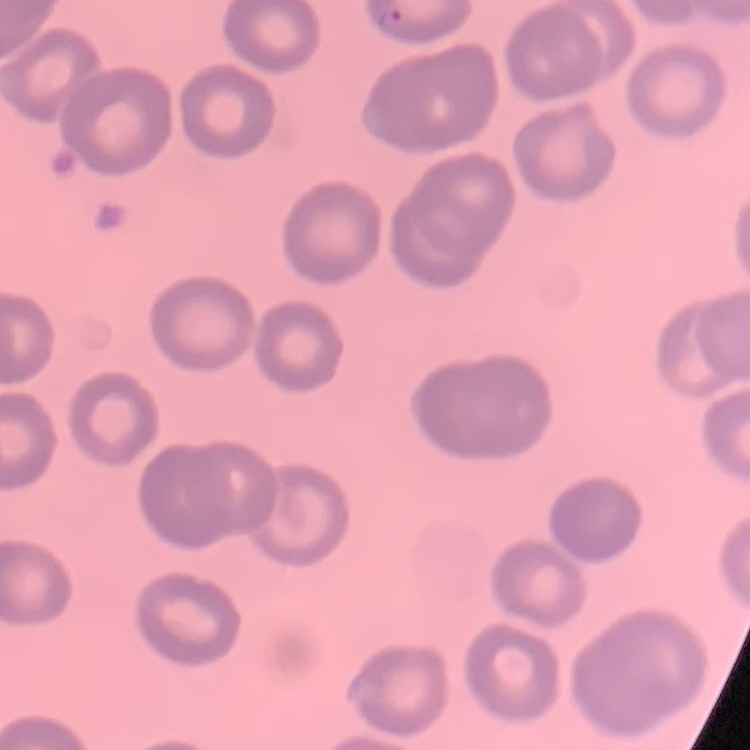
The red blood cells exhibit no rouleaux formation. Thin peripheral smear. Field's or Giemsa stain. Square crop of a larger photomicrograph.